Give the position of every leukocyte.
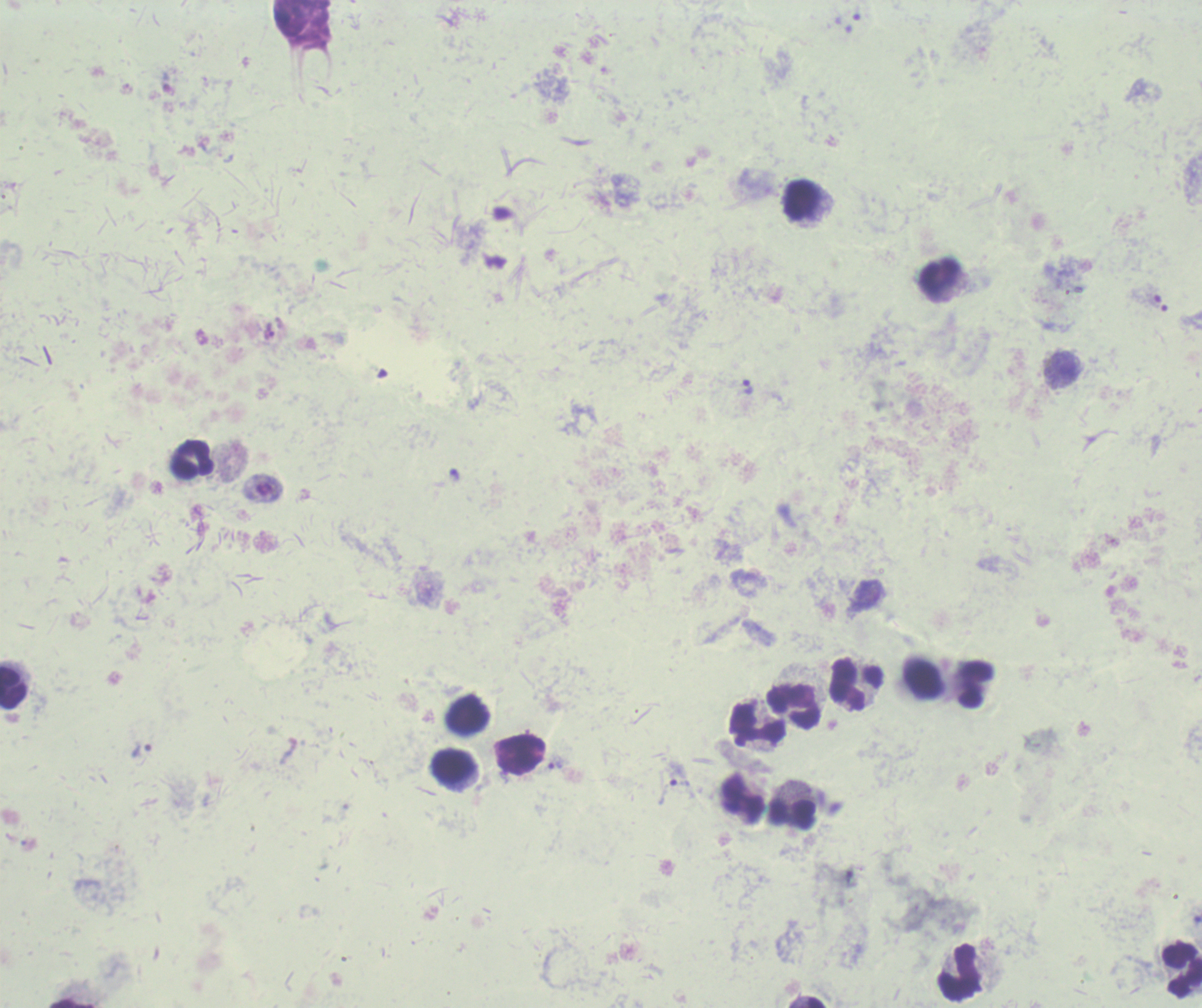

Approximate object centers, in pixels from the top-left corner.
Leukocytes: (x=802, y=198), (x=940, y=276), (x=193, y=459), (x=922, y=678), (x=856, y=684), (x=976, y=685), (x=13, y=687), (x=793, y=706), (x=469, y=716), (x=756, y=724), (x=522, y=754), (x=453, y=767), (x=745, y=799), (x=792, y=813), (x=1182, y=970), (x=958, y=972), (x=71, y=1003), (x=816, y=1003).

context: previously used in an actual diagnosis
trophozoite_locations: 'approximate object centers, in pixels from the top-left corner: (x=853, y=24), (x=269, y=331), (x=748, y=387), (x=142, y=751), (x=556, y=763), (x=678, y=773)'
magnification: 100x
image_size: 1202×1008 pixels
result: positive for Plasmodium parasites
field_of_view: single
preparation: thick blood smear
background_quality: poor
stain: Romanowsky